Classify this cell by malaria status.
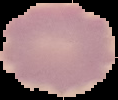
It is uninfected.

From a thin blood film. Segmented cell region on a black background. Image is 118×100 pixels.